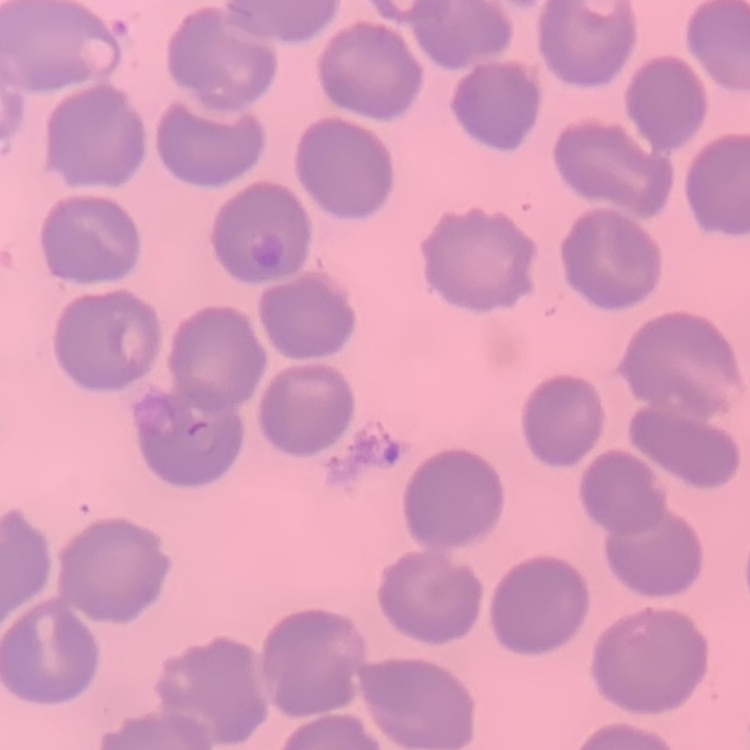
Summary:
  - Erythrocyte morphology: no rouleaux formation
  - Image type: one tile cut from a larger photomicrograph
  - Stain: Field's or Giemsa
  - Preparation: thin blood smear